Report the malaria status of this cell.
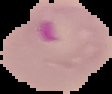
It is parasitized.

From a thin blood smear. Cell region segmented out of the field of view; the surrounding area is masked to black. Image is 112×94 pixels.